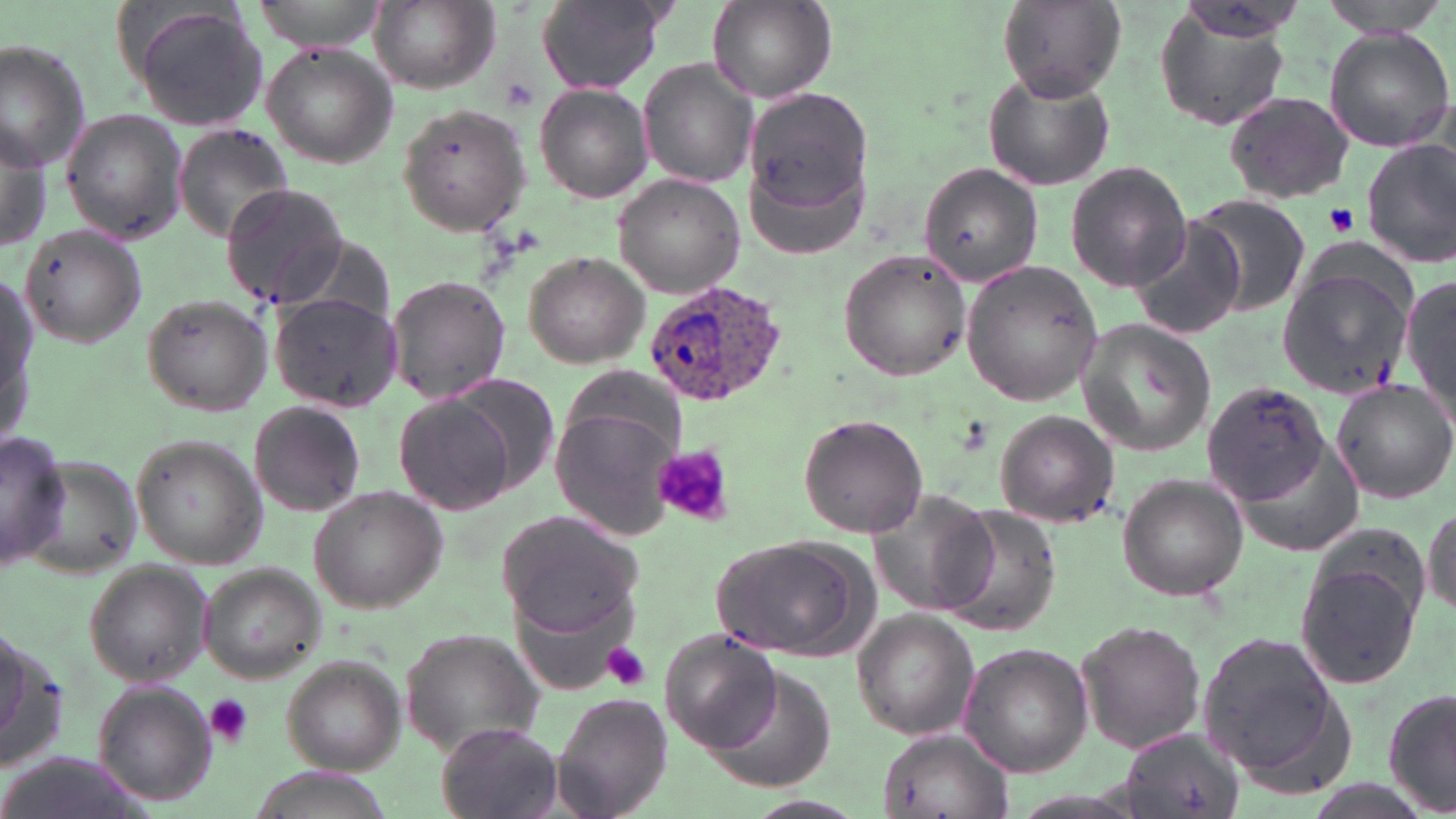

Summary:
  - Coordinate format: approximate bounding boxes as (x1, y1, x2, y2) in pixels
  - Platelet locations: (496, 77, 539, 115), (1326, 203, 1357, 236), (653, 444, 733, 527), (602, 642, 653, 691), (204, 694, 254, 746)
  - Uninfected red blood cell locations: (244, 0, 395, 50), (536, 0, 667, 92), (997, 0, 1125, 100), (1319, 0, 1453, 34), (369, 1, 498, 91), (706, 2, 835, 104), (127, 4, 273, 134), (1154, 9, 1296, 133), (1324, 27, 1455, 152), (0, 40, 93, 170), (262, 43, 397, 169), (639, 59, 759, 188), (982, 68, 1115, 190), (535, 84, 653, 203), (744, 90, 876, 228), (1223, 90, 1353, 203), (397, 103, 533, 236), (61, 108, 188, 246), (1, 117, 51, 253), (172, 124, 297, 243), (1363, 139, 1456, 267), (1064, 162, 1193, 295), (917, 163, 1042, 286), (614, 175, 744, 298), (219, 183, 349, 312), (1191, 195, 1310, 316), (1127, 217, 1247, 341), (19, 225, 147, 349), (838, 249, 970, 379), (522, 251, 650, 368), (961, 261, 1104, 405), (0, 264, 42, 456), (1276, 267, 1414, 397), (386, 275, 511, 403), (1401, 276, 1456, 415), (269, 293, 405, 414), (138, 294, 273, 417), (1077, 318, 1216, 458), (447, 378, 561, 494), (1330, 379, 1456, 503), (1202, 383, 1330, 502), (392, 394, 514, 516), (250, 402, 365, 515), (551, 408, 679, 538), (995, 409, 1118, 528), (798, 414, 929, 536), (0, 430, 69, 573), (130, 432, 265, 571), (1118, 474, 1248, 601), (307, 486, 447, 613), (870, 487, 999, 619), (1423, 501, 1456, 618), (935, 504, 1060, 635), (496, 509, 648, 640), (715, 535, 867, 659), (1294, 545, 1427, 694), (83, 559, 214, 685), (196, 565, 328, 686), (853, 611, 980, 739), (1075, 618, 1206, 756), (0, 621, 71, 769), (400, 626, 545, 756), (1193, 628, 1351, 789), (660, 629, 778, 752), (958, 642, 1096, 777), (280, 656, 405, 774), (706, 666, 837, 794), (92, 681, 216, 807), (1384, 685, 1456, 817), (552, 693, 671, 819), (436, 721, 561, 819), (877, 727, 1015, 819), (1118, 729, 1243, 818), (238, 768, 401, 819)
  - Plasmodium ovale-infected red blood cell locations: (643, 281, 791, 409)
  - Slide-level diagnosis: Plasmodium ovale
  - Image size: 1456×819 pixels
  - Magnification: 1000x
  - Modality: light microscopy
  - Field of view: one of a larger specimen
  - Preparation: thin blood film
  - Stain: May-Grünwald-Giemsa